Locate and identify every blood parasite.
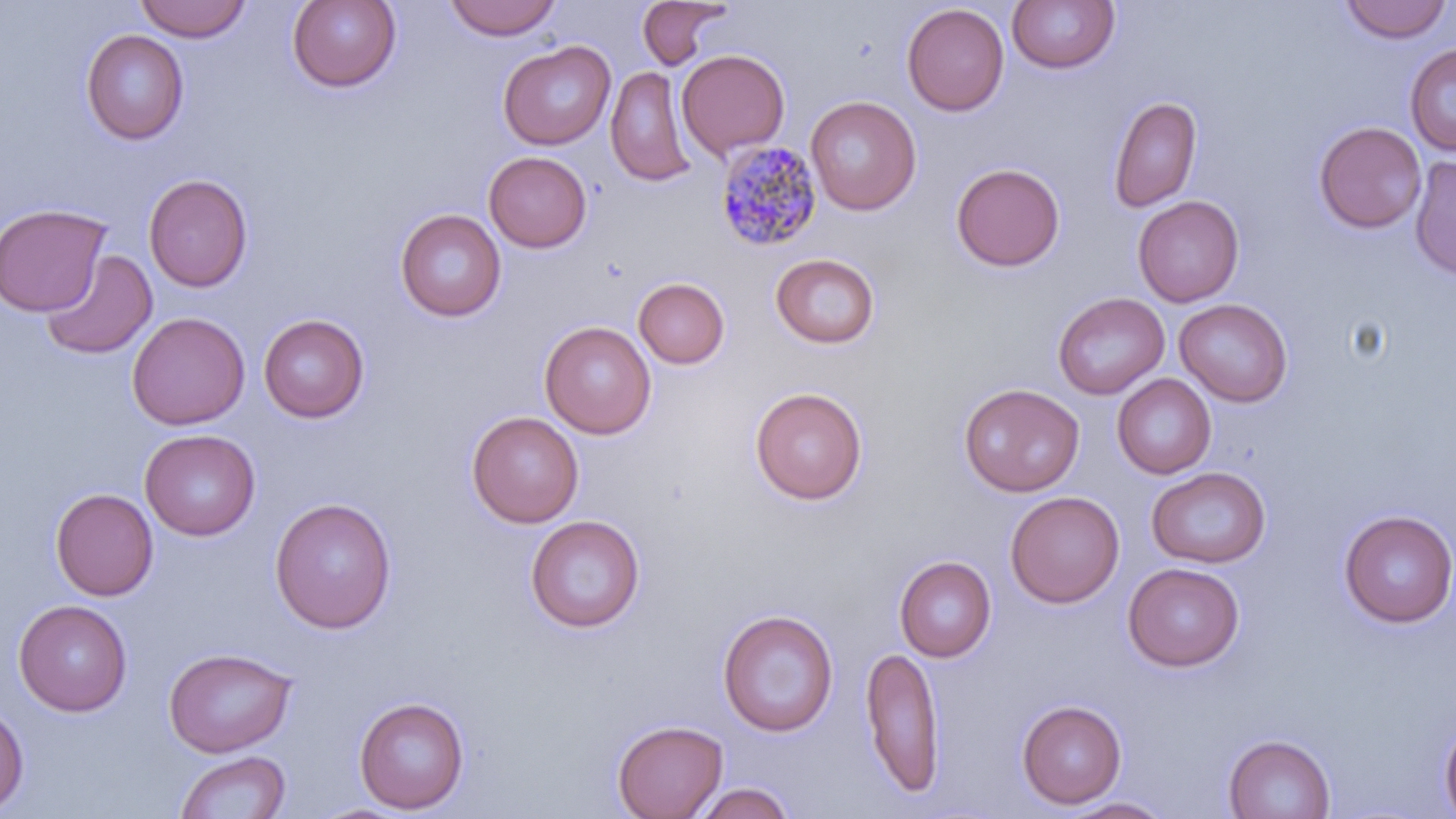
Approximate bounding boxes as named x1/y1/x2/y2 corners in pixels.
Plasmodium malariae-infected red blood cells: (x1=714, y1=140, x2=824, y2=255).
No Plasmodium falciparum, Plasmodium ovale, Plasmodium vivax, Babesia divergens, or Trypanosoma brucei observed.

slide-level diagnosis = Plasmodium malariae
preparation = thin blood film
field of view = single
stain = May-Grünwald-Giemsa
image size = 1456×819 pixels
uninfected red blood cell locations = approximate bounding boxes as named x1/y1/x2/y2 corners in pixels: (x1=135, y1=0, x2=252, y2=43), (x1=287, y1=0, x2=402, y2=93), (x1=444, y1=0, x2=562, y2=41), (x1=636, y1=0, x2=734, y2=70), (x1=1007, y1=0, x2=1120, y2=75), (x1=1339, y1=1, x2=1453, y2=44), (x1=902, y1=3, x2=1009, y2=116), (x1=81, y1=28, x2=189, y2=144), (x1=498, y1=40, x2=615, y2=150), (x1=1405, y1=44, x2=1456, y2=156), (x1=676, y1=49, x2=790, y2=159), (x1=605, y1=65, x2=699, y2=188), (x1=805, y1=95, x2=921, y2=215), (x1=1108, y1=95, x2=1202, y2=214), (x1=1313, y1=121, x2=1426, y2=234), (x1=484, y1=151, x2=592, y2=252), (x1=1408, y1=155, x2=1456, y2=280), (x1=951, y1=162, x2=1065, y2=272), (x1=143, y1=173, x2=253, y2=292), (x1=1132, y1=195, x2=1244, y2=307), (x1=0, y1=203, x2=111, y2=317), (x1=395, y1=208, x2=507, y2=322), (x1=40, y1=249, x2=157, y2=360), (x1=770, y1=253, x2=881, y2=348), (x1=633, y1=277, x2=730, y2=369), (x1=1052, y1=291, x2=1170, y2=399), (x1=1174, y1=298, x2=1293, y2=407), (x1=127, y1=312, x2=250, y2=430), (x1=258, y1=314, x2=370, y2=423), (x1=539, y1=321, x2=656, y2=439), (x1=1112, y1=374, x2=1216, y2=478), (x1=958, y1=383, x2=1084, y2=497), (x1=750, y1=386, x2=868, y2=504), (x1=466, y1=410, x2=584, y2=528), (x1=140, y1=429, x2=261, y2=540), (x1=1146, y1=466, x2=1271, y2=568), (x1=50, y1=488, x2=159, y2=600), (x1=1005, y1=491, x2=1125, y2=608), (x1=269, y1=497, x2=397, y2=634), (x1=1338, y1=509, x2=1456, y2=628), (x1=525, y1=515, x2=645, y2=633), (x1=894, y1=555, x2=997, y2=662), (x1=1122, y1=562, x2=1245, y2=671), (x1=13, y1=599, x2=132, y2=716), (x1=717, y1=608, x2=839, y2=737), (x1=859, y1=644, x2=945, y2=800), (x1=163, y1=647, x2=297, y2=757), (x1=354, y1=696, x2=469, y2=814), (x1=1016, y1=699, x2=1127, y2=809), (x1=0, y1=701, x2=29, y2=813), (x1=1439, y1=714, x2=1456, y2=818), (x1=611, y1=719, x2=728, y2=819), (x1=1223, y1=733, x2=1336, y2=818), (x1=175, y1=749, x2=291, y2=819), (x1=690, y1=782, x2=797, y2=819), (x1=1059, y1=796, x2=1174, y2=818), (x1=308, y1=802, x2=412, y2=818)
magnification = 1000x
modality = light microscopy